Identify the blood parasite species.
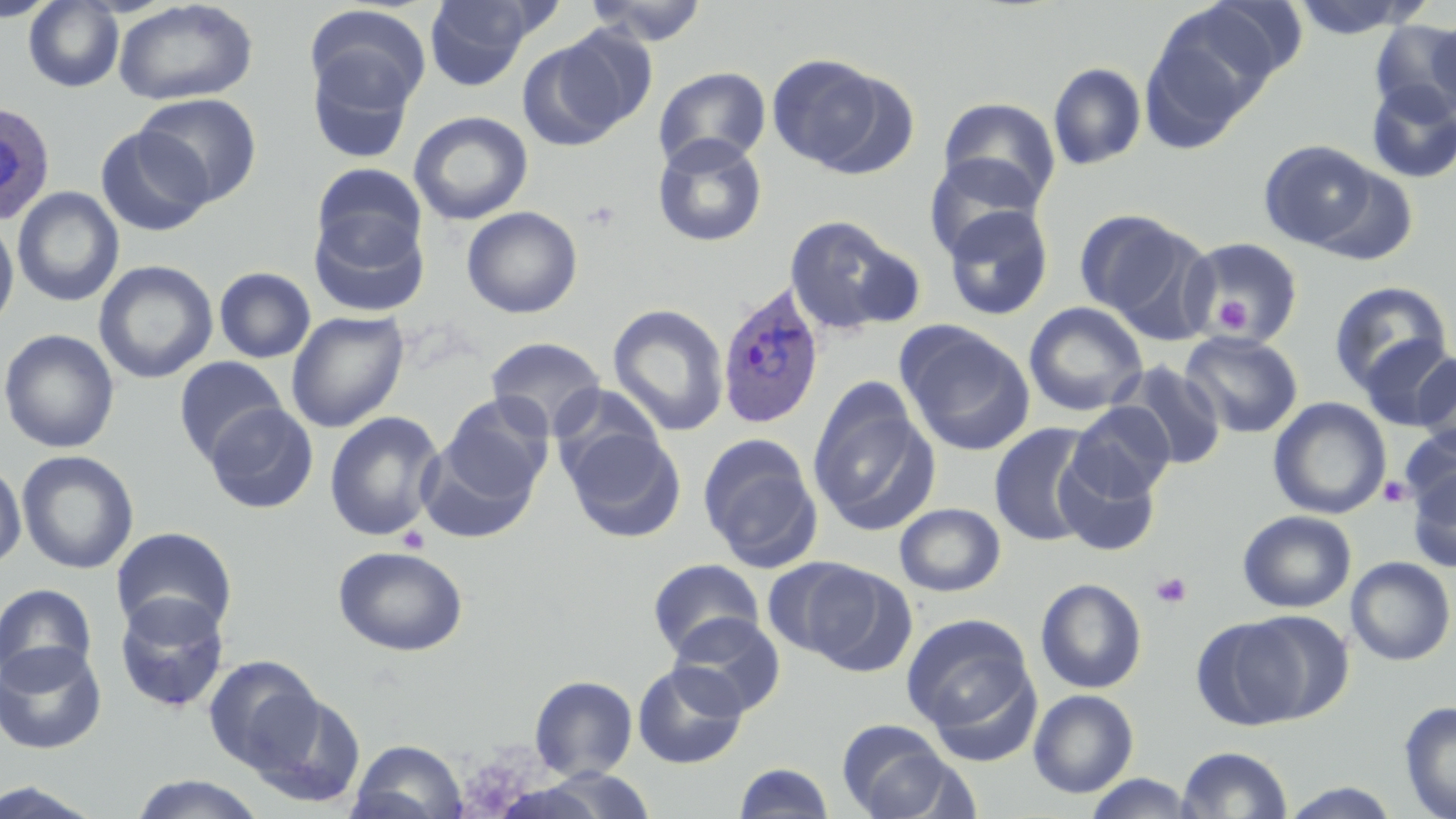
Plasmodium ovale.

image size = 1456×819 pixels
Plasmodium ovale-infected red blood cell locations = approximate bounding boxes as (x1,y1)-(x2,y2) corner pairs in pixels: (0,100)-(56,226), (714,283)-(826,431)
preparation = thin blood film
modality = optical microscopy
magnification = 1000x
field of view = single
stain = May-Grünwald-Giemsa
uninfected red blood cell locations = approximate bounding boxes as (x1,y1)-(x2,y2) corner pairs in pixels: (0,0)-(59,22), (23,0)-(125,92), (112,0)-(259,106), (423,0)-(542,89), (583,0)-(710,47), (1289,0)-(1424,39), (1190,2)-(1310,87), (307,6)-(432,119), (1142,10)-(1272,146), (1430,17)-(1456,113), (1370,19)-(1456,120), (529,28)-(653,142), (305,48)-(418,164), (767,53)-(887,171), (1048,62)-(1147,170), (653,67)-(772,171), (1365,81)-(1456,184), (135,93)-(263,206), (937,97)-(1062,209), (408,110)-(533,226), (95,125)-(212,237), (652,135)-(768,247), (1258,140)-(1379,249), (924,154)-(1043,260), (312,163)-(427,265), (1307,164)-(1420,267), (12,187)-(124,307), (942,203)-(1054,320), (461,206)-(583,318), (1075,208)-(1188,319), (309,210)-(430,317), (783,214)-(921,337), (0,218)-(19,333), (1104,224)-(1220,348), (1180,235)-(1304,346), (94,260)-(218,384), (214,267)-(316,363), (1328,280)-(1453,395), (1024,301)-(1148,417), (607,304)-(730,436), (286,310)-(409,433), (896,322)-(1035,456), (0,329)-(120,453), (1180,331)-(1304,438), (1356,334)-(1456,431), (485,336)-(607,439), (1413,354)-(1456,455), (173,356)-(288,466), (1115,361)-(1227,471), (807,379)-(939,537), (550,385)-(666,490), (438,395)-(555,506), (1268,397)-(1391,519), (1069,402)-(1175,501), (204,403)-(318,514), (324,411)-(446,541), (989,423)-(1100,546), (1399,425)-(1456,519), (563,426)-(686,543), (417,434)-(543,544), (698,436)-(823,573), (16,450)-(139,575), (1054,452)-(1160,556), (0,462)-(27,570), (1407,468)-(1455,573), (895,503)-(1005,597), (1238,510)-(1356,613), (111,526)-(237,639), (332,545)-(469,656), (1346,556)-(1455,666), (648,559)-(764,660), (788,560)-(915,675), (1035,578)-(1147,693), (0,581)-(100,687), (114,593)-(231,713), (1236,611)-(1355,723), (667,612)-(786,717), (901,614)-(1036,735), (1190,618)-(1311,733), (0,642)-(107,754), (203,654)-(323,773), (632,661)-(748,769), (921,662)-(1046,769), (529,675)-(638,780), (246,689)-(366,806), (1028,689)-(1139,798), (1399,700)-(1456,819), (835,719)-(962,819), (347,739)-(468,819), (1176,746)-(1293,818), (732,761)-(836,818), (1081,773)-(1201,818), (127,774)-(269,818), (1,779)-(107,818), (1277,782)-(1406,817)
platelet locations = approximate bounding boxes as (x1,y1)-(x2,y2) corner pairs in pixels: (581,199)-(622,233), (1213,295)-(1252,334), (1378,475)-(1412,507), (1151,571)-(1193,608)